Locate every malaria parasite.
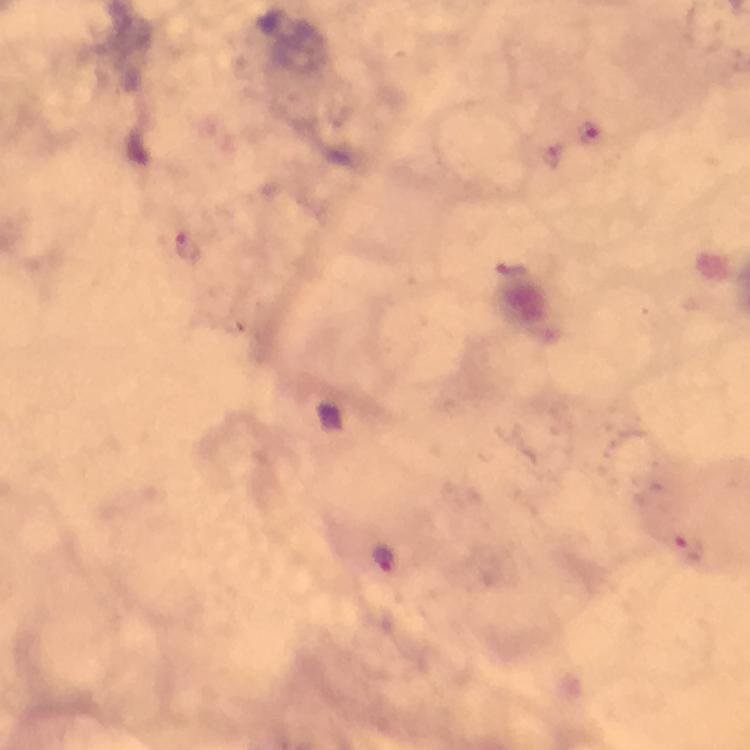
Approximate centers as (x, y) in pixels.
Malaria parasites: (591, 135), (184, 250), (687, 546), (384, 556).

Image is 750×750 pixels. Photographed through the microscope with a smartphone camera. Cropped region of a single field of view. Giemsa stain. Immersion oil applied. Thick blood smear. At 100x magnification. From a diagnostic examination for malaria.